Report the malaria status of this cell.
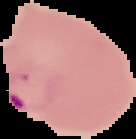
Parasitized.

Summary:
  - Image type: segmented cell region with the area outside set to black
  - Preparation: thin blood film
  - Image size: 136×139 pixels